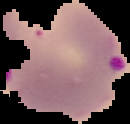

{
  "image_type": "segmented cell region on a black background",
  "malaria_status": "parasitized",
  "preparation": "thin blood smear",
  "image_size": "130×124 pixels"
}